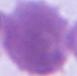

Micrograph. 1000x magnification. An erythrocyte is shown.